Assess this cell for malaria.
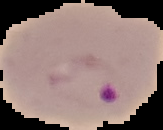
Parasitized.

Segmented cell region on a black background. From a thin blood smear. Image is 163×130 pixels.